Classify this cell by malaria status.
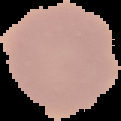

It is uninfected.

Image is 121×121 pixels. Segmented cell region on a black background. From a thin blood smear.